Report the malaria status of this cell.
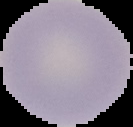

It is uninfected.

From a thin blood smear. Segmented cell region on a black background. Image is 133×127 pixels.